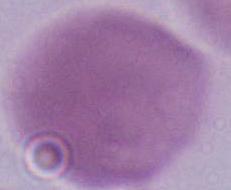 Captured at 1000x magnification. Micrograph. A red blood cell is seen.